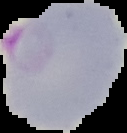
Segmented cell region on a black background. From a thin blood smear. Malaria status: parasitized. Image is 127×133 pixels.